Give the position of every malaria parasite.
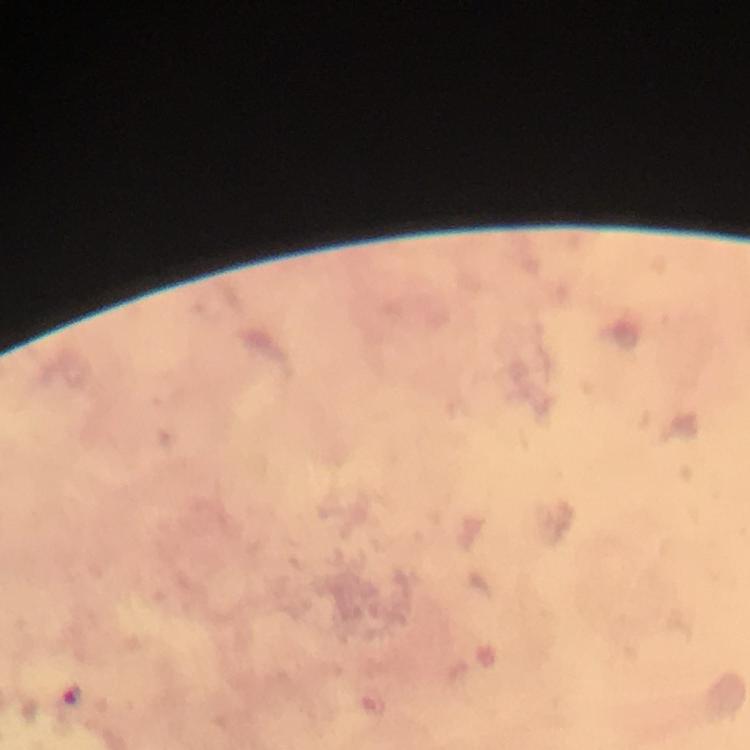
Approximate object centers, in pixels from the top-left corner.
Malaria parasites: (x=74, y=696).

Summary:
  - Capture: smartphone camera through the microscope
  - Context: from a diagnostic examination for malaria
  - Preparation: thick blood smear
  - Image size: 750×750 pixels
  - Immersion oil: used
  - Cropped from: one field of view
  - Magnification: 100x
  - Stain: Giemsa